Classify this cell by malaria status.
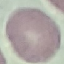

Uninfected.

Summary:
  - Image type: cell patch, automatically extracted from a larger field of view and resized to 64 × 64 pixels
  - Capture: smartphone through the microscope eyepiece
  - Preparation: thin blood film
  - Stain: Giemsa